Name the parasite shown.
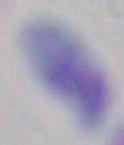

This is Toxoplasma gondii.

Photomicrograph. Captured at 1000x magnification.